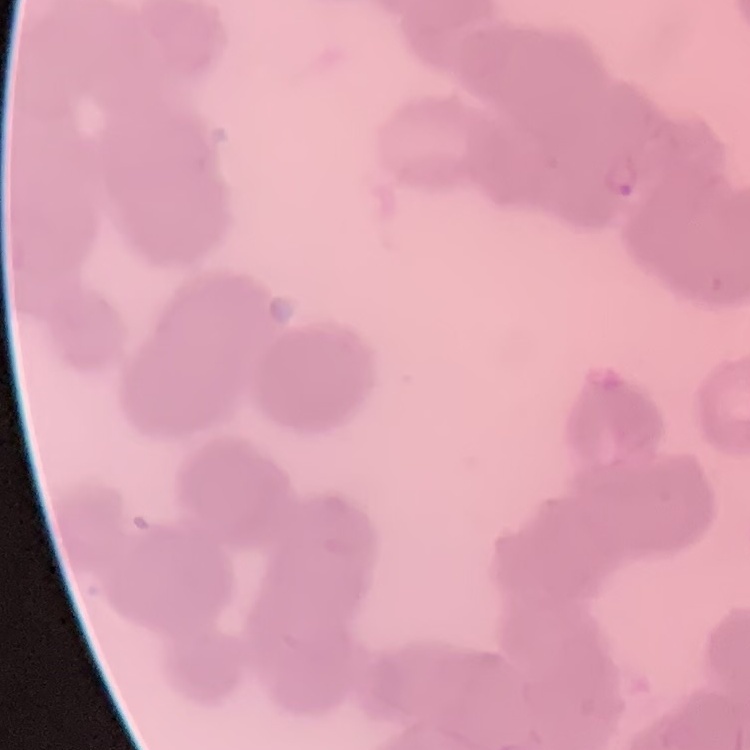 The red blood cells exhibit rouleaux formation. Thin blood film. Square crop of a larger photomicrograph. Field's or Giemsa stain.